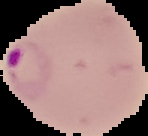
{
  "image_size": "148×136 pixels",
  "result": "Plasmodium parasites detected",
  "preparation": "thin blood film",
  "image_type": "segmented cell region with the area outside set to black"
}